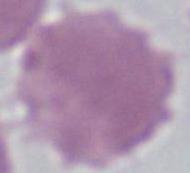
magnification = 1000x
identification = erythrocyte
modality = photomicrograph